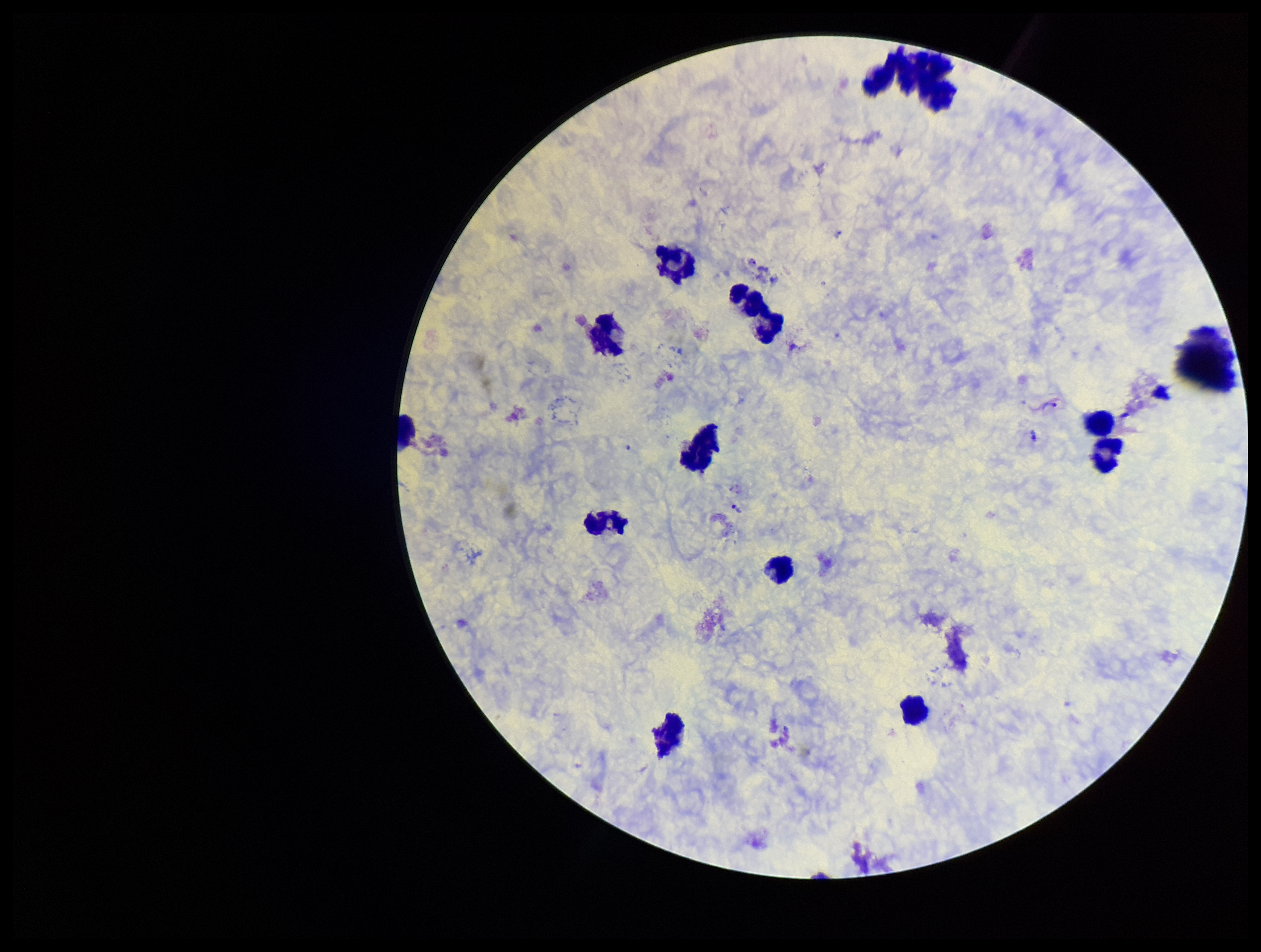 Preparation: thick. Species reported for this patient: Plasmodium vivax. Leukocyte count: 12. Plasmodium parasites: detected. Image is 1261×952 pixels. Stained with Giemsa. One field from this slide. Parasite count: 5. Patient malaria status: infected. Smartphone photograph taken through the eyepiece of a microscope.